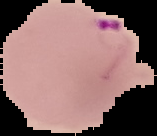

result = Plasmodium parasites detected
image size = 157×136 pixels
preparation = thin blood smear
image type = cell region segmented out of the field of view; surrounding area masked to black